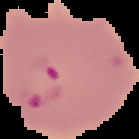

image size = 139×139 pixels
image type = segmented cell region on a black background
result = malaria parasites detected
preparation = thin blood film